Name the parasite shown.
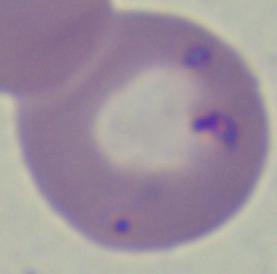

Babesia.

Micrograph. 1000x magnification.